Locate every blood parasite and identify its species.
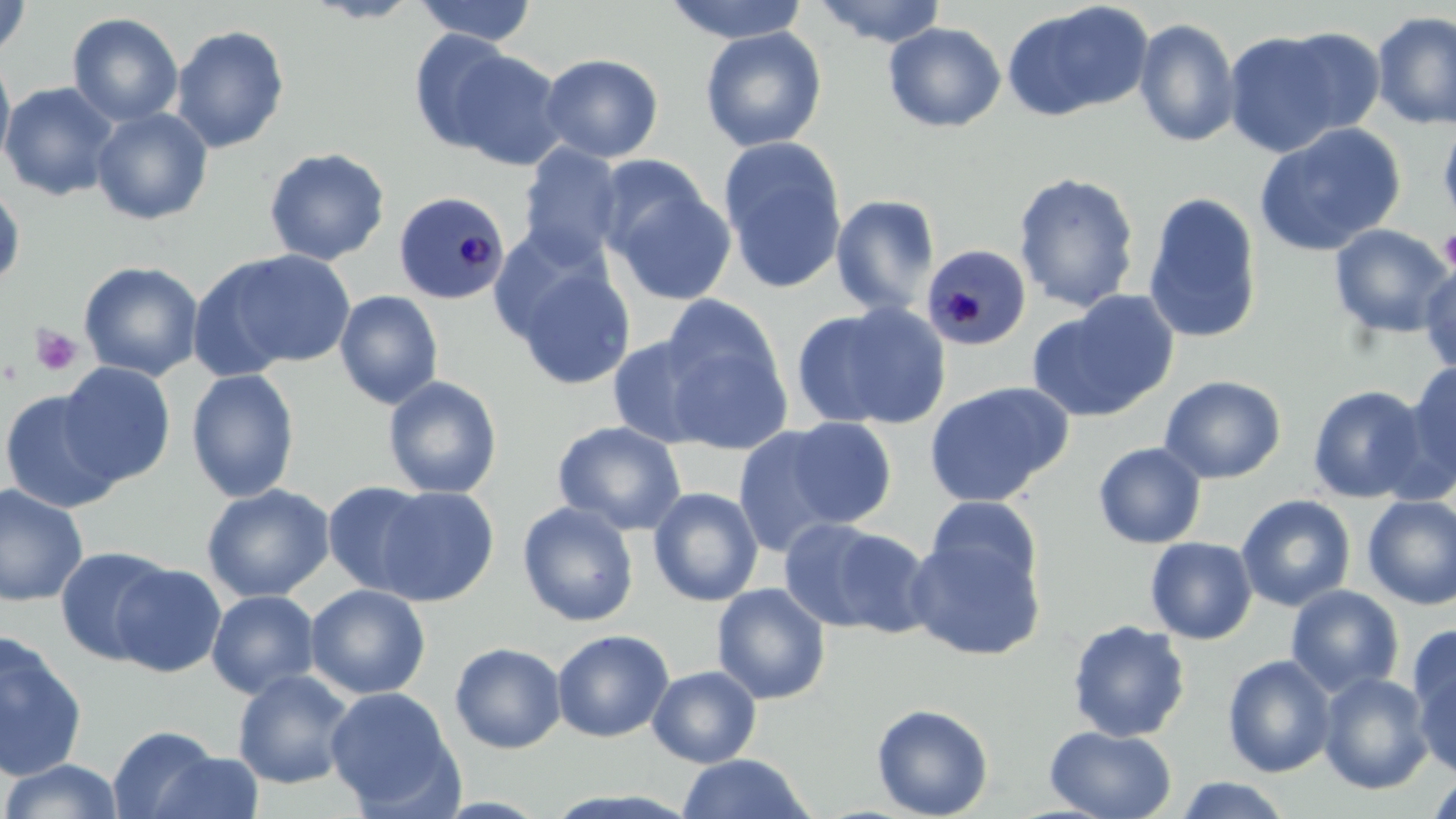
Approximate bounding boxes as (x1, y1, x2, y2) in pixels.
Plasmodium malariae-infected red blood cells: (392, 190, 511, 305), (920, 242, 1032, 351).
No Plasmodium falciparum, Plasmodium ovale, Plasmodium vivax, Babesia divergens, or Trypanosoma brucei observed.

Uninfected red blood cell locations: (0, 0, 32, 61), (304, 0, 424, 23), (413, 0, 538, 46), (661, 0, 812, 44), (812, 0, 949, 47), (1000, 1, 1154, 122), (1371, 10, 1456, 130), (67, 12, 183, 127), (1134, 18, 1241, 147), (883, 22, 1007, 133), (170, 24, 290, 153), (700, 26, 827, 152), (1270, 27, 1388, 137), (408, 29, 520, 154), (1221, 29, 1354, 157), (446, 50, 569, 171), (0, 53, 16, 176), (539, 53, 663, 163), (0, 81, 118, 201), (91, 107, 214, 226), (1437, 117, 1456, 234), (1254, 122, 1407, 257), (719, 137, 848, 296), (518, 143, 626, 265), (263, 147, 391, 266), (602, 171, 737, 306), (1012, 171, 1141, 313), (0, 183, 26, 291), (1142, 191, 1264, 345), (830, 194, 940, 316), (1329, 224, 1454, 339), (207, 248, 359, 372), (1418, 257, 1456, 377), (78, 260, 204, 381), (511, 264, 637, 391), (334, 290, 444, 410), (1029, 292, 1180, 423), (793, 301, 952, 431), (660, 324, 794, 455), (607, 334, 722, 449), (58, 361, 176, 486), (1405, 361, 1456, 488), (185, 368, 300, 503), (382, 375, 503, 499), (1159, 375, 1286, 484), (923, 380, 1073, 508), (1306, 384, 1430, 504), (0, 388, 124, 513), (783, 416, 898, 528), (552, 420, 687, 536), (732, 426, 847, 558), (1093, 442, 1206, 549), (321, 480, 436, 596), (0, 482, 89, 606), (201, 483, 336, 603), (373, 485, 499, 606), (647, 487, 764, 607), (1235, 494, 1356, 612), (1361, 495, 1456, 610), (925, 496, 1043, 594), (517, 501, 639, 627), (777, 517, 909, 634), (905, 534, 1046, 661), (1144, 536, 1258, 644), (54, 546, 175, 666), (111, 562, 227, 678), (711, 583, 831, 705), (305, 584, 430, 699), (1285, 584, 1404, 697), (206, 589, 320, 699), (1066, 619, 1192, 743), (1408, 624, 1456, 726), (551, 629, 674, 742), (0, 635, 88, 782), (449, 641, 567, 754), (1222, 654, 1337, 777), (1412, 662, 1456, 780), (647, 665, 762, 768), (232, 669, 357, 789), (1317, 672, 1434, 794), (325, 686, 461, 815), (871, 703, 994, 819), (107, 724, 224, 819), (1044, 724, 1177, 819), (150, 752, 267, 818), (676, 753, 813, 818), (1, 758, 126, 818), (1425, 771, 1456, 819), (1174, 776, 1295, 818). Platelet locations: (1439, 227, 1456, 273), (29, 326, 84, 377). Slide-level diagnosis: Plasmodium malariae. Light microscopy. Single field of view. Image is 1456×819 pixels. Thin blood smear. May-Grünwald-Giemsa-stained preparation. Captured at 1000x magnification.